Assess this cell for malaria.
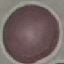
Uninfected.

Automatically extracted cell patch, resized to 64 × 64 pixels. Thin smear of blood. Giemsa stain. Acquired by smartphone through the microscope eyepiece.